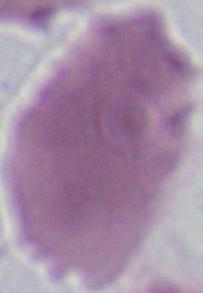

{
  "identification": "red blood cell",
  "modality": "micrograph",
  "magnification": "1000x"
}